Classify this cell by malaria status.
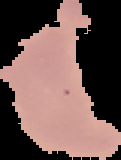

Uninfected.

Summary:
  - Image size: 121×160 pixels
  - Image type: cell region segmented out of the field of view; surrounding area masked to black
  - Preparation: thin blood smear